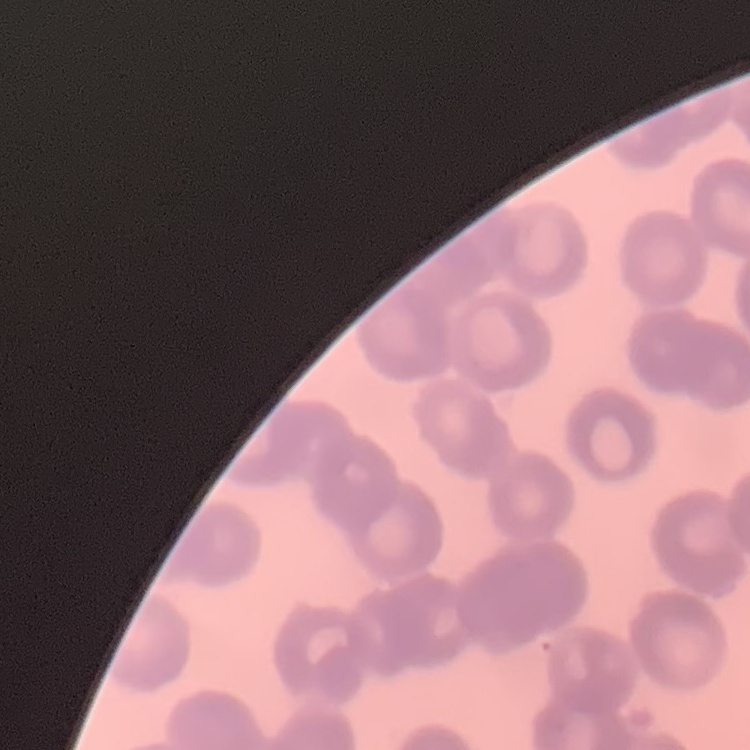

erythrocyte morphology = no rouleaux formation
image type = one tile cut from a larger photomicrograph
preparation = thin blood film
stain = Field's or Giemsa